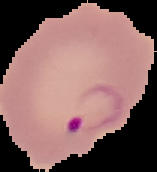
result = Plasmodium parasites detected
preparation = thin blood film
image type = segmented cell region on a black background
image size = 157×172 pixels